Describe the morphology of the erythrocytes.
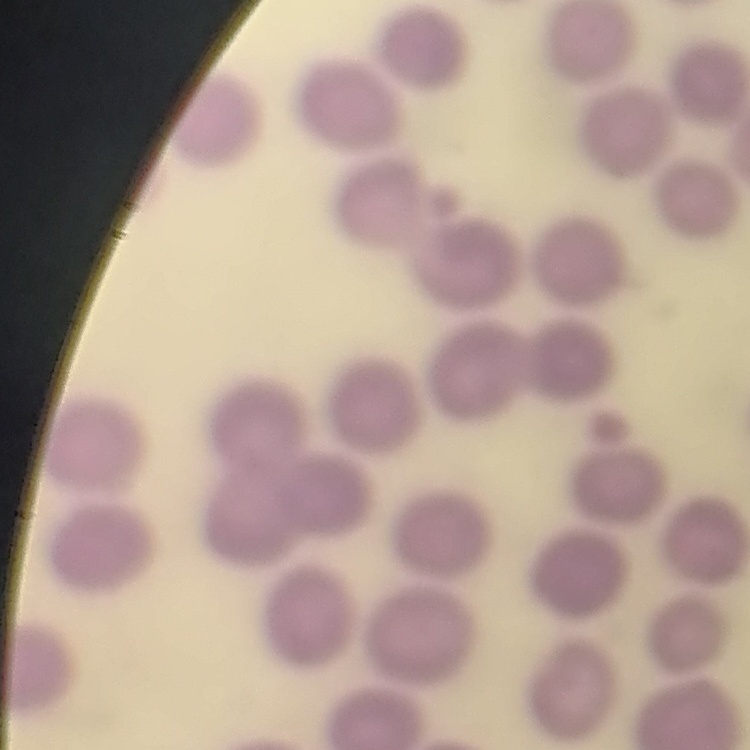

No rouleaux formation.

Summary:
  - Preparation: thin blood film
  - Image type: square crop of a larger photomicrograph
  - Stain: Field's or Giemsa